Identify the parasite.
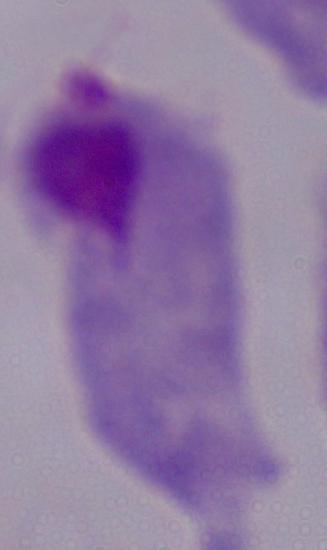

This is a trichomonad.

{
  "magnification": "1000x",
  "modality": "micrograph"
}